Classify this cell by malaria status.
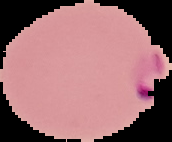
Parasitized.

Summary:
  - Preparation: thin blood film
  - Image type: segmented cell region on a black background
  - Image size: 172×142 pixels